Locate and identify every blood parasite.
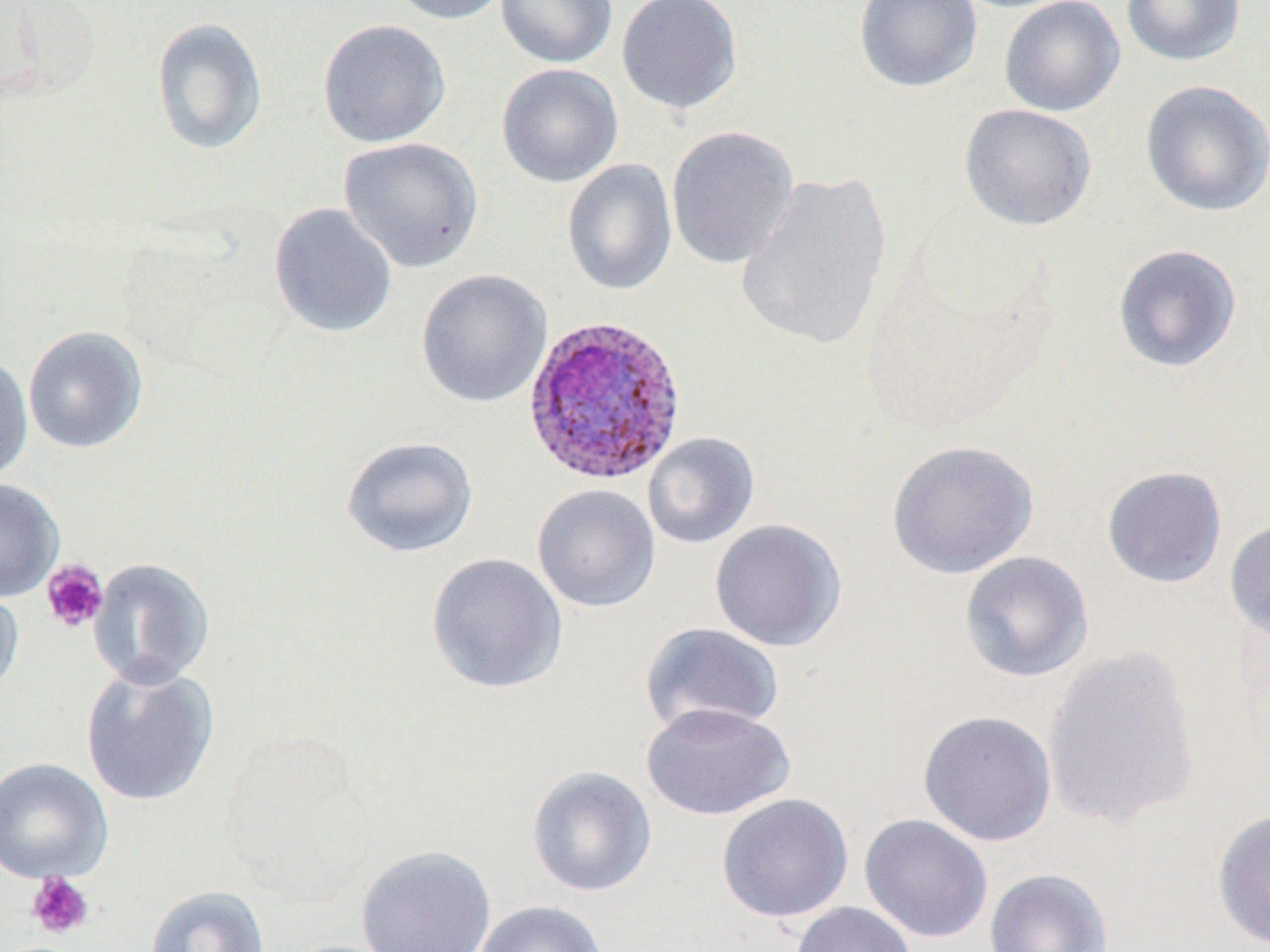
Approximate bounding boxes as named x1/y1/x2/y2 corners in pixels.
Plasmodium ovale-infected red blood cells: (x1=521, y1=314, x2=688, y2=488).
No Plasmodium falciparum, Plasmodium malariae, Plasmodium vivax, Babesia divergens, or Trypanosoma brucei observed.

slide_level_diagnosis: Plasmodium ovale
uninfected_red_blood_cell_locations: 'approximate bounding boxes as named x1/y1/x2/y2 corners in pixels: (x1=387, y1=0, x2=513, y2=25), (x1=495, y1=0, x2=618, y2=68), (x1=616, y1=0, x2=743, y2=116), (x1=853, y1=0, x2=983, y2=93), (x1=999, y1=0, x2=1125, y2=117), (x1=1120, y1=0, x2=1246, y2=67), (x1=150, y1=16, x2=269, y2=155), (x1=316, y1=18, x2=451, y2=148), (x1=496, y1=63, x2=623, y2=188), (x1=1139, y1=79, x2=1270, y2=217), (x1=959, y1=104, x2=1097, y2=231), (x1=666, y1=125, x2=799, y2=270), (x1=338, y1=137, x2=485, y2=273), (x1=562, y1=158, x2=677, y2=296), (x1=736, y1=172, x2=893, y2=352), (x1=268, y1=202, x2=398, y2=338), (x1=1112, y1=244, x2=1242, y2=373), (x1=415, y1=268, x2=552, y2=409), (x1=22, y1=326, x2=149, y2=454), (x1=0, y1=353, x2=33, y2=484), (x1=642, y1=432, x2=760, y2=549), (x1=340, y1=435, x2=479, y2=558), (x1=885, y1=439, x2=1039, y2=579), (x1=1101, y1=465, x2=1228, y2=589), (x1=0, y1=478, x2=65, y2=602), (x1=531, y1=484, x2=661, y2=613), (x1=1225, y1=517, x2=1270, y2=645), (x1=709, y1=518, x2=847, y2=652), (x1=958, y1=550, x2=1094, y2=683), (x1=426, y1=552, x2=569, y2=695), (x1=87, y1=557, x2=215, y2=689), (x1=0, y1=581, x2=24, y2=700), (x1=639, y1=622, x2=786, y2=738), (x1=1041, y1=645, x2=1201, y2=831), (x1=80, y1=663, x2=219, y2=807), (x1=640, y1=701, x2=796, y2=821), (x1=917, y1=710, x2=1057, y2=847), (x1=0, y1=757, x2=113, y2=885), (x1=525, y1=765, x2=657, y2=897), (x1=716, y1=793, x2=854, y2=923), (x1=1211, y1=807, x2=1270, y2=950), (x1=858, y1=813, x2=993, y2=943), (x1=355, y1=844, x2=497, y2=952), (x1=984, y1=868, x2=1113, y2=952), (x1=143, y1=884, x2=271, y2=952), (x1=472, y1=900, x2=607, y2=952), (x1=790, y1=901, x2=917, y2=952)'
image_size: 1270×952 pixels
modality: optical microscopy
field_of_view: one of a larger specimen
platelet_locations: 'approximate bounding boxes as named x1/y1/x2/y2 corners in pixels: (x1=41, y1=558, x2=109, y2=634), (x1=25, y1=872, x2=95, y2=939)'
magnification: 1000x
stain: May-Grünwald-Giemsa
preparation: thin blood smear